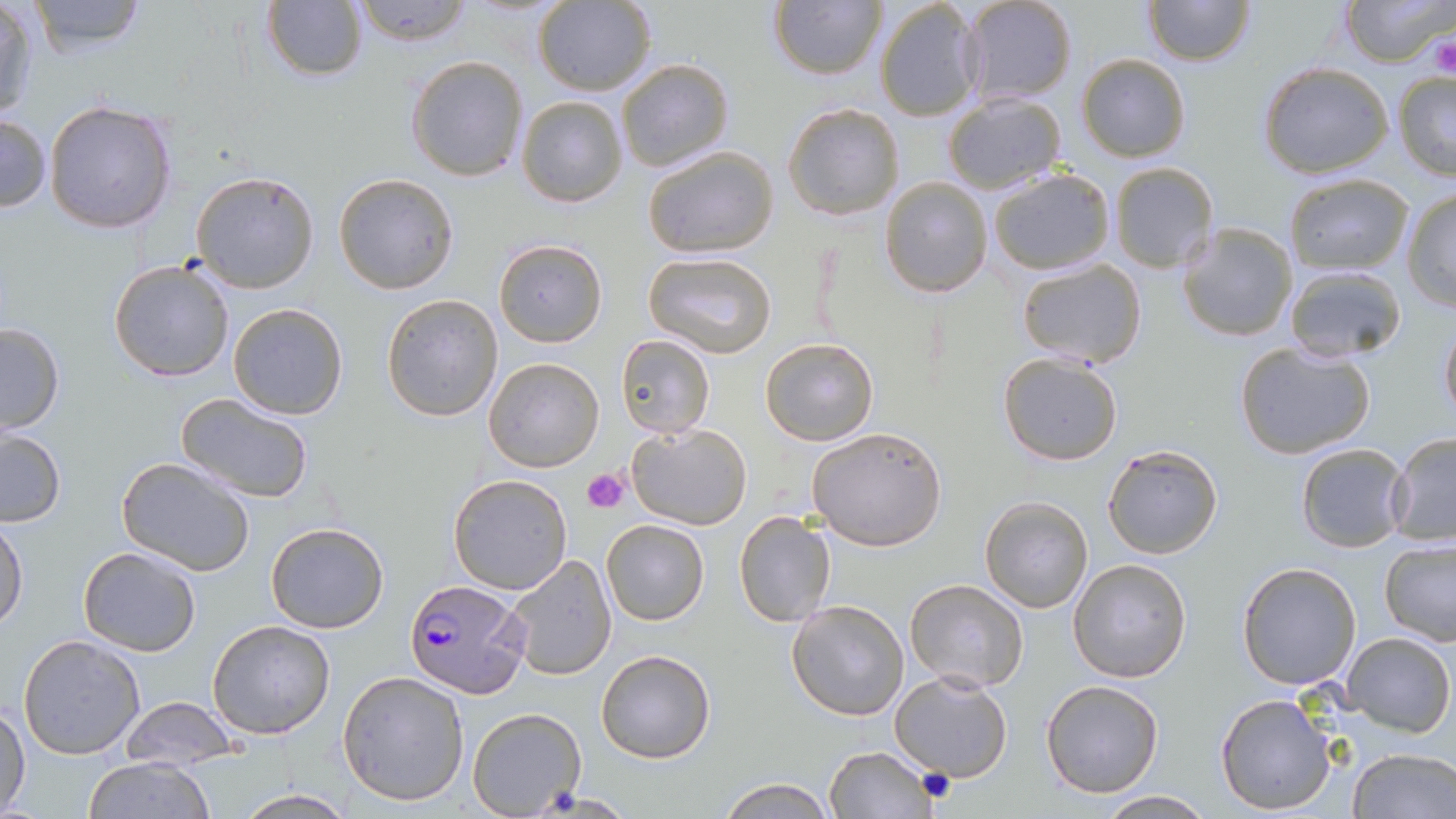 Approximate bounding boxes as (x1, y1, x2, y2) in pixels. Uninfected red blood cell locations: (25, 0, 151, 55), (352, 0, 472, 46), (533, 0, 655, 96), (769, 0, 886, 81), (959, 0, 1078, 108), (1144, 0, 1255, 66), (1342, 0, 1453, 66), (260, 1, 369, 82), (873, 1, 983, 122), (1, 2, 42, 123), (1077, 53, 1189, 163), (406, 54, 528, 182), (617, 59, 734, 172), (1258, 61, 1393, 179), (1392, 70, 1456, 178), (941, 92, 1067, 195), (517, 96, 628, 207), (45, 98, 177, 233), (782, 103, 905, 221), (0, 113, 50, 213), (642, 144, 779, 258), (1110, 163, 1219, 275), (191, 170, 320, 294), (986, 170, 1113, 275), (333, 173, 459, 294), (1284, 174, 1413, 273), (881, 176, 991, 296), (1401, 188, 1456, 312), (1177, 222, 1298, 342), (493, 239, 607, 347), (644, 251, 778, 358), (108, 259, 237, 383), (1015, 259, 1146, 367), (1282, 265, 1409, 364), (381, 294, 503, 423), (227, 303, 347, 420), (1439, 318, 1456, 426), (0, 322, 65, 434), (615, 334, 716, 437), (761, 337, 878, 446), (1232, 340, 1376, 461), (998, 352, 1125, 466), (483, 355, 605, 473), (172, 393, 317, 506), (627, 423, 751, 530), (806, 425, 949, 551), (0, 430, 65, 526), (1386, 432, 1456, 547), (1295, 442, 1412, 552), (1102, 445, 1223, 559), (116, 455, 256, 577), (448, 474, 572, 594), (979, 496, 1093, 613), (733, 509, 837, 628), (0, 518, 28, 628), (602, 519, 709, 625), (265, 522, 390, 633), (1378, 539, 1456, 649), (77, 546, 202, 657), (499, 555, 616, 681), (1067, 557, 1193, 683), (1236, 562, 1362, 689), (905, 579, 1030, 693), (786, 599, 910, 720), (208, 619, 336, 738), (1344, 631, 1455, 736), (17, 634, 146, 759), (594, 647, 718, 764), (337, 670, 469, 807), (889, 670, 1015, 783), (1040, 680, 1164, 799), (1215, 691, 1337, 815), (121, 697, 239, 770), (1, 705, 30, 816), (466, 707, 585, 817), (823, 745, 937, 818), (1344, 746, 1455, 819), (82, 757, 215, 819), (718, 776, 833, 817), (235, 787, 352, 818), (1097, 791, 1216, 817). Plasmodium falciparum-infected red blood cell locations: (406, 579, 529, 698). Platelet locations: (1431, 38, 1455, 82), (584, 466, 632, 514), (918, 768, 955, 803). Slide-level diagnosis: Plasmodium falciparum. Image is 1456×819 pixels. Light microscopy. Single field of view. Thin blood film. May-Grünwald-Giemsa stain. Captured at 1000x magnification.